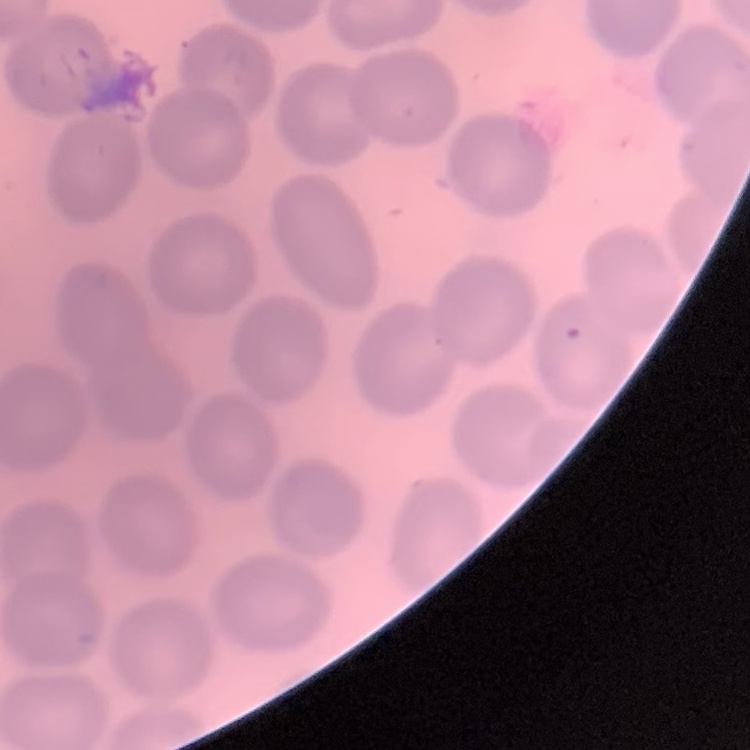

erythrocyte morphology = no rouleaux formation
image type = one tile cut from a larger photomicrograph
stain = Field's or Giemsa
preparation = thin blood film